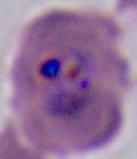
Photomicrograph. 400x or 1000x magnification. A Plasmodium parasite is shown.